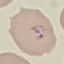
Summary:
  - Result: malaria parasites identified
  - Image type: automatically extracted cell patch, resized to 64 × 64 pixels
  - Capture: smartphone through the microscope eyepiece
  - Stain: Giemsa
  - Preparation: thin smear